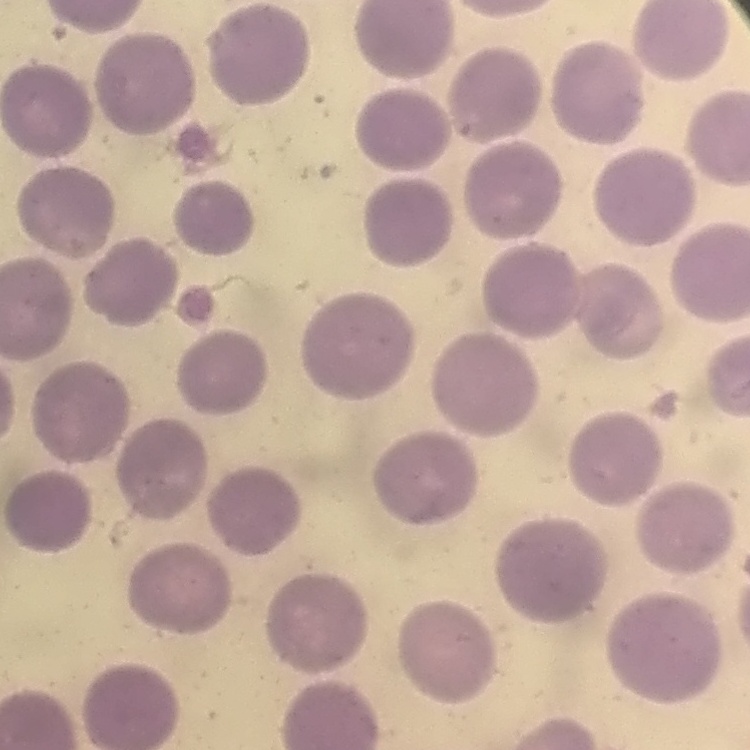
red blood cell morphology = no rouleaux formation
image type = square crop of a larger photomicrograph
stain = Field's or Giemsa
preparation = thin blood film